Comment on the morphology of the red blood cells.
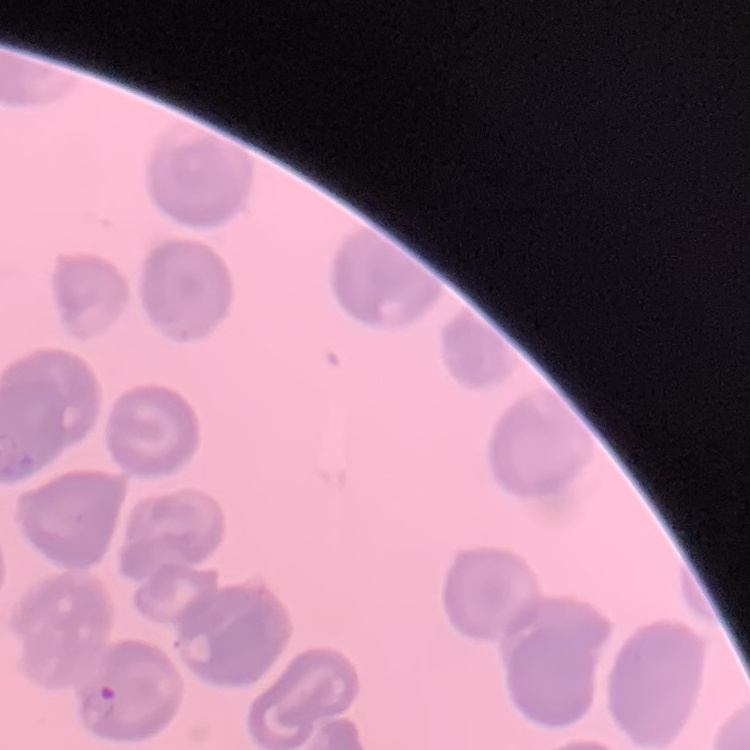
No rouleaux formation.

stain: Field's or Giemsa
image_type: square crop of a larger photomicrograph
preparation: thin blood smear